Locate the Plasmodium falciparum-infected red blood cells and any of indeterminate infection status.
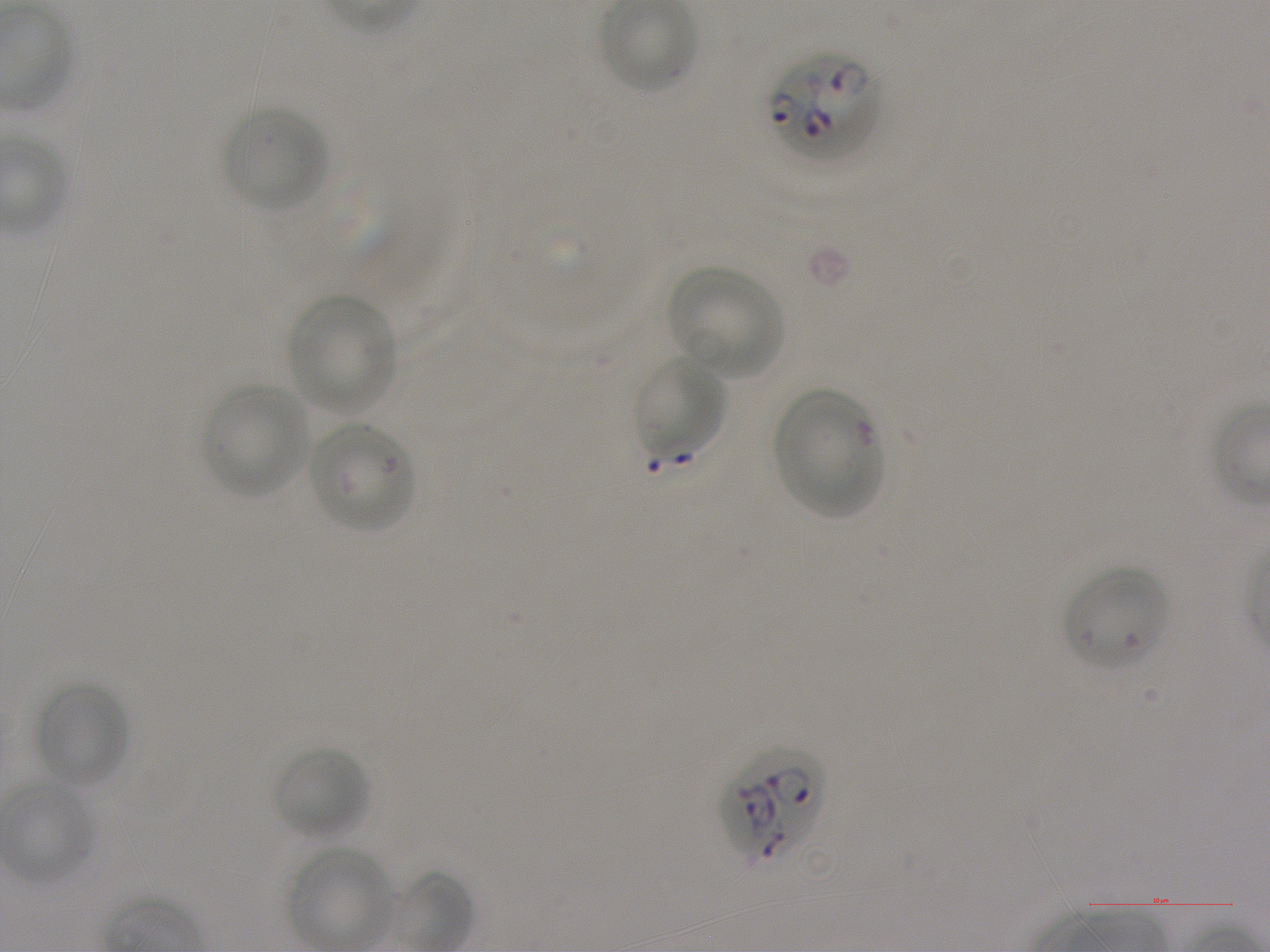

Approximate bounding boxes as {x1, y1, x2, y2} in pixels. Not every red blood cell is marked.
Infected red blood cells: {768, 53, 880, 163}, {721, 747, 824, 867}.
Red blood cells of indeterminate infection status: {772, 385, 881, 518}, {1063, 566, 1170, 672}.

Summary:
  - Locations of uninfected red blood cells: {599, 0, 697, 94}, {222, 106, 328, 212}, {667, 266, 783, 380}, {288, 294, 395, 414}, {634, 356, 727, 461}, {202, 383, 311, 499}, {309, 422, 417, 531}, {34, 681, 129, 789}, {271, 746, 370, 840}, {3, 782, 96, 885}, {290, 847, 390, 950}
  - Preparation: thin blood film
  - Objective: 100x, oil immersion, numerical aperture 1.25
  - Donor blood group: A+
  - Stain: Giemsa
  - Field of view: one from this slide
  - Image size: 1270×952 pixels
  - Culture: in-vitro Plasmodium falciparum strain NF54, static